Describe the morphology of the erythrocytes.
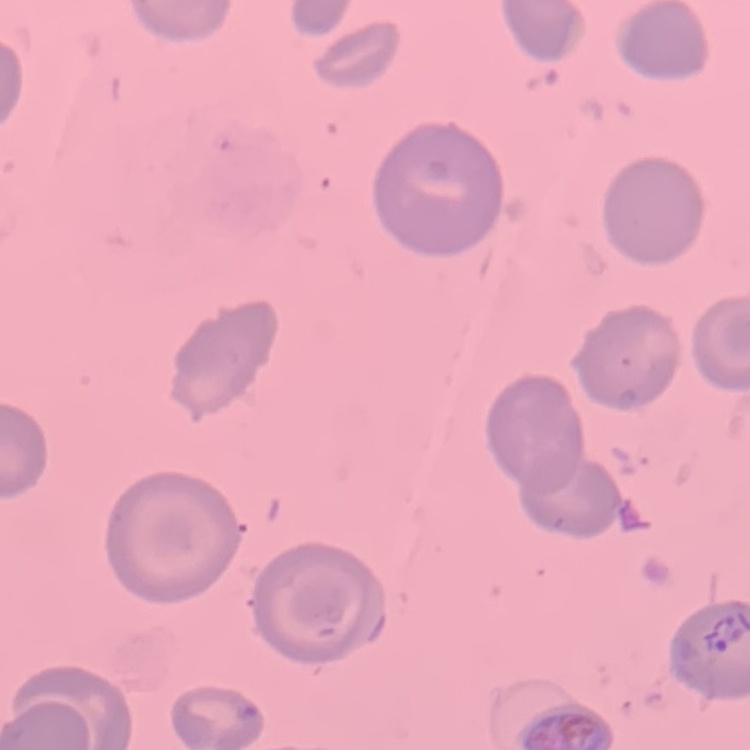

They show no rouleaux formation.

Summary:
  - Image type: square crop of a larger photomicrograph
  - Stain: Field's or Giemsa
  - Preparation: thin peripheral smear